Report the malaria status of this cell.
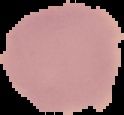

Uninfected.

Image is 124×115 pixels. The area outside the segmented cell region is set to black. From a thin blood smear.